Outline each blood parasite and name the species.
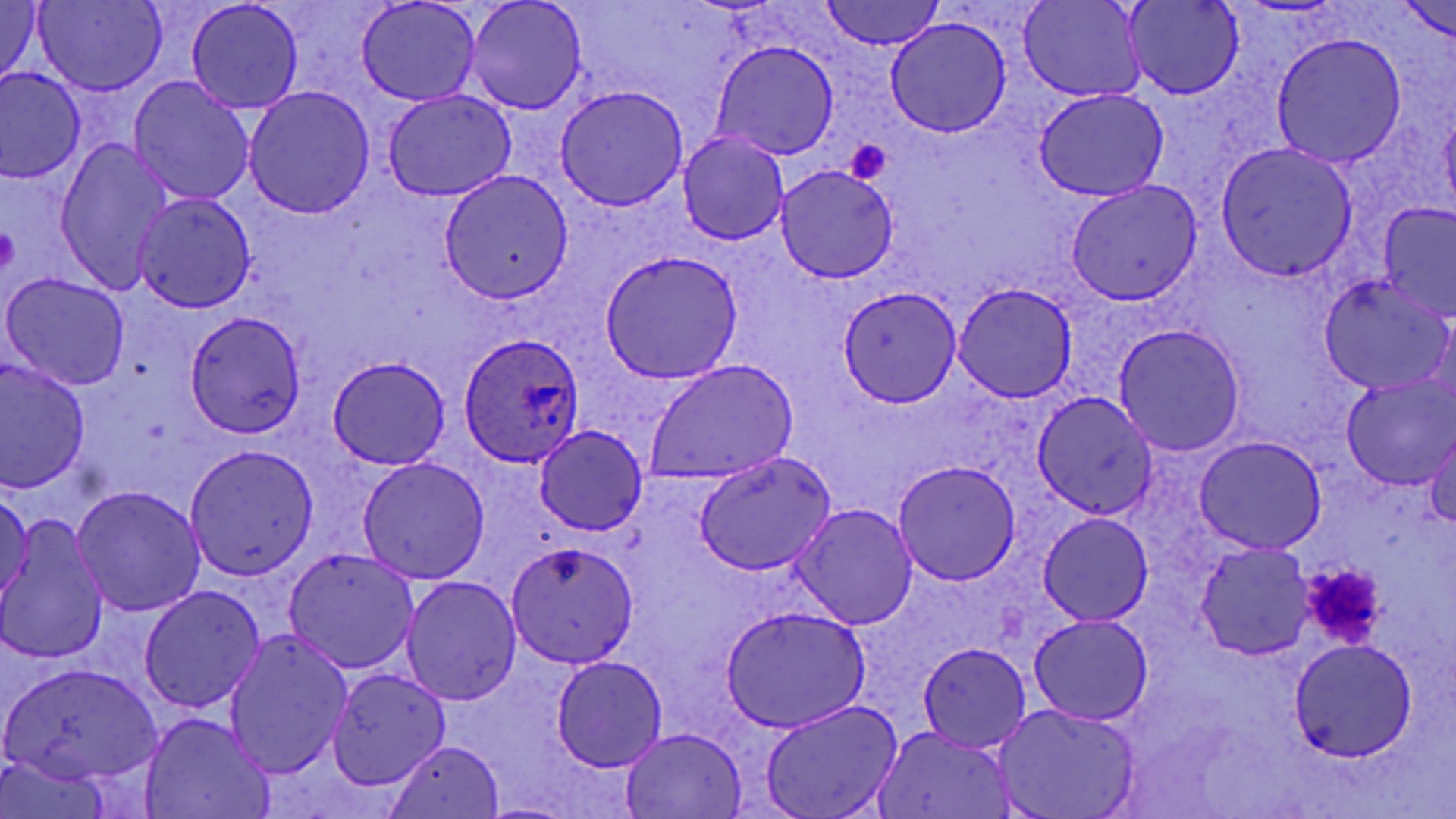

Approximate bounding boxes as named x1/y1/x2/y2 corners in pixels.
Plasmodium ovale-infected red blood cells: (x1=459, y1=333, x2=584, y2=467).
No Plasmodium falciparum, Plasmodium malariae, Plasmodium vivax, Babesia divergens, or Trypanosoma brucei observed.

slide-level diagnosis = Plasmodium ovale
platelet locations = approximate bounding boxes as named x1/y1/x2/y2 corners in pixels: (x1=844, y1=136, x2=892, y2=183), (x1=1, y1=222, x2=19, y2=277), (x1=1300, y1=562, x2=1388, y2=648)
preparation = thin blood film
magnification = 1000x
modality = light microscopy
uninfected red blood cell locations = approximate bounding boxes as named x1/y1/x2/y2 corners in pixels: (x1=357, y1=0, x2=479, y2=106), (x1=466, y1=0, x2=586, y2=115), (x1=820, y1=0, x2=943, y2=51), (x1=1122, y1=0, x2=1243, y2=100), (x1=34, y1=1, x2=164, y2=96), (x1=187, y1=1, x2=303, y2=113), (x1=1018, y1=1, x2=1145, y2=102), (x1=0, y1=2, x2=47, y2=90), (x1=1399, y1=3, x2=1455, y2=45), (x1=885, y1=16, x2=1011, y2=138), (x1=1269, y1=35, x2=1406, y2=168), (x1=711, y1=41, x2=838, y2=161), (x1=0, y1=69, x2=86, y2=181), (x1=129, y1=77, x2=254, y2=205), (x1=556, y1=85, x2=689, y2=209), (x1=243, y1=86, x2=375, y2=218), (x1=1035, y1=88, x2=1169, y2=202), (x1=383, y1=90, x2=514, y2=201), (x1=1439, y1=107, x2=1456, y2=215), (x1=679, y1=132, x2=788, y2=244), (x1=54, y1=137, x2=174, y2=292), (x1=1215, y1=144, x2=1357, y2=283), (x1=776, y1=164, x2=898, y2=282), (x1=439, y1=171, x2=573, y2=303), (x1=1065, y1=182, x2=1201, y2=305), (x1=131, y1=192, x2=256, y2=313), (x1=1377, y1=202, x2=1456, y2=324), (x1=598, y1=251, x2=742, y2=382), (x1=1, y1=272, x2=131, y2=390), (x1=1319, y1=277, x2=1454, y2=394), (x1=952, y1=284, x2=1078, y2=402), (x1=837, y1=286, x2=963, y2=407), (x1=184, y1=310, x2=307, y2=438), (x1=1113, y1=325, x2=1246, y2=455), (x1=327, y1=358, x2=451, y2=469), (x1=1, y1=359, x2=90, y2=495), (x1=644, y1=360, x2=799, y2=483), (x1=1342, y1=375, x2=1456, y2=489), (x1=1032, y1=393, x2=1159, y2=520), (x1=534, y1=425, x2=648, y2=535), (x1=1425, y1=425, x2=1456, y2=528), (x1=1196, y1=436, x2=1327, y2=554), (x1=185, y1=444, x2=319, y2=581), (x1=695, y1=451, x2=836, y2=577), (x1=357, y1=456, x2=491, y2=584), (x1=892, y1=461, x2=1021, y2=586), (x1=71, y1=485, x2=206, y2=617), (x1=0, y1=488, x2=34, y2=605), (x1=791, y1=503, x2=918, y2=630), (x1=1038, y1=512, x2=1153, y2=626), (x1=1, y1=521, x2=110, y2=665), (x1=504, y1=540, x2=641, y2=667), (x1=1196, y1=542, x2=1315, y2=659), (x1=283, y1=548, x2=420, y2=673), (x1=401, y1=576, x2=523, y2=704), (x1=139, y1=585, x2=266, y2=714), (x1=718, y1=606, x2=873, y2=734), (x1=1030, y1=614, x2=1152, y2=725), (x1=224, y1=631, x2=352, y2=778), (x1=1288, y1=639, x2=1417, y2=763), (x1=919, y1=640, x2=1032, y2=753), (x1=551, y1=655, x2=668, y2=772), (x1=5, y1=662, x2=163, y2=786), (x1=327, y1=668, x2=450, y2=790), (x1=759, y1=699, x2=900, y2=819), (x1=995, y1=704, x2=1140, y2=818), (x1=140, y1=713, x2=276, y2=818), (x1=874, y1=725, x2=1013, y2=819), (x1=619, y1=726, x2=748, y2=818), (x1=382, y1=740, x2=507, y2=818)
stain = May-Grünwald-Giemsa
field of view = single
image size = 1456×819 pixels